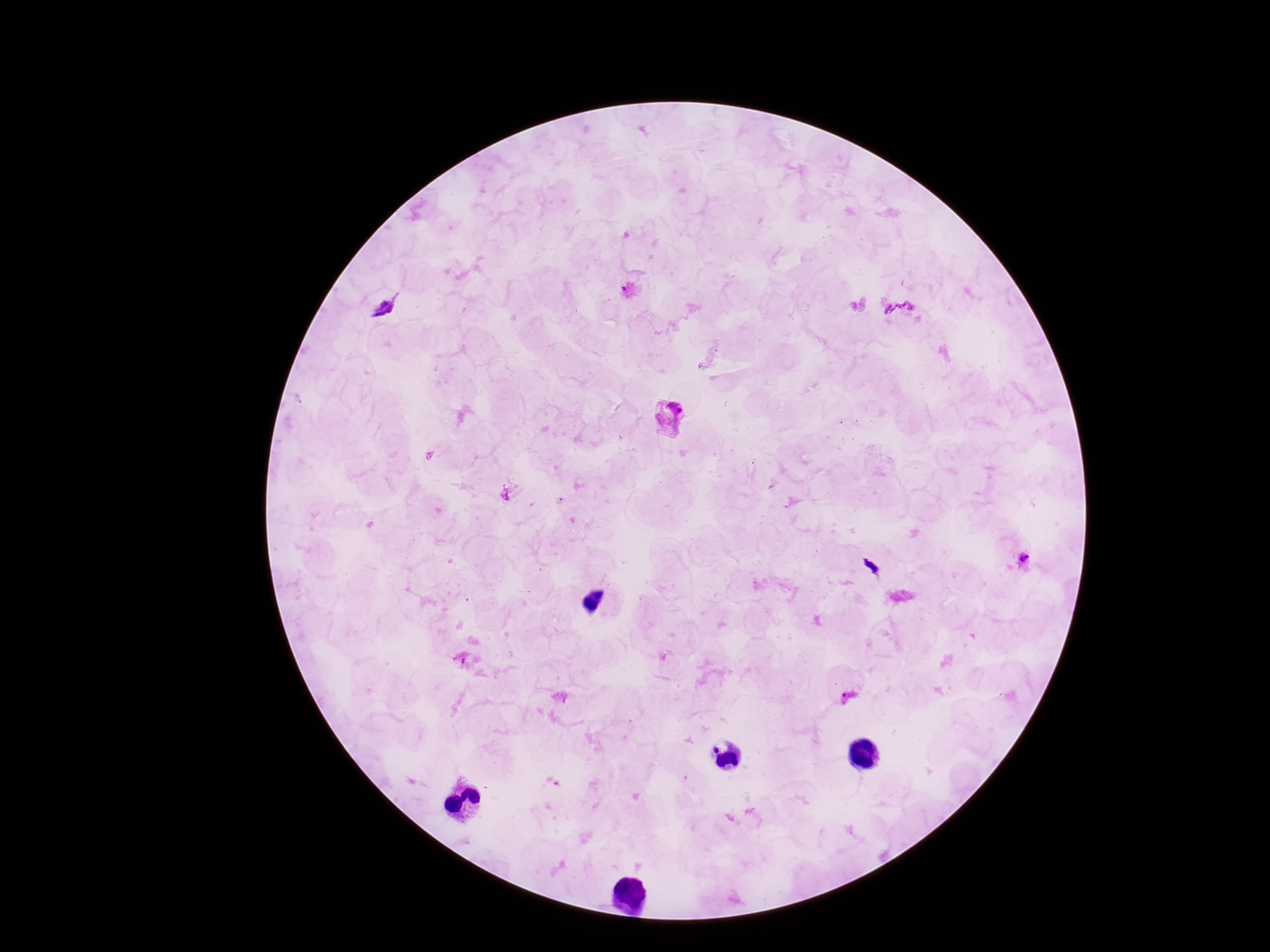 Approximate centers as (x, y) in pixels. Plasmodium parasite locations: (900, 310), (669, 420), (509, 497), (1022, 559), (463, 660), (846, 692). One field from this slide. Thick blood film. 100x magnification. Photographed through the microscope eyepiece with a smartphone camera. Patient malaria status: infected. Image is 1270×952 pixels. Giemsa-stained preparation.